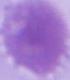 Captured at 1000x magnification. An erythrocyte is shown. Micrograph.